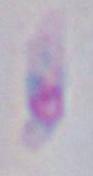

{
  "modality": "photomicrograph",
  "magnification": "1000x",
  "identification": "Toxoplasma gondii"
}